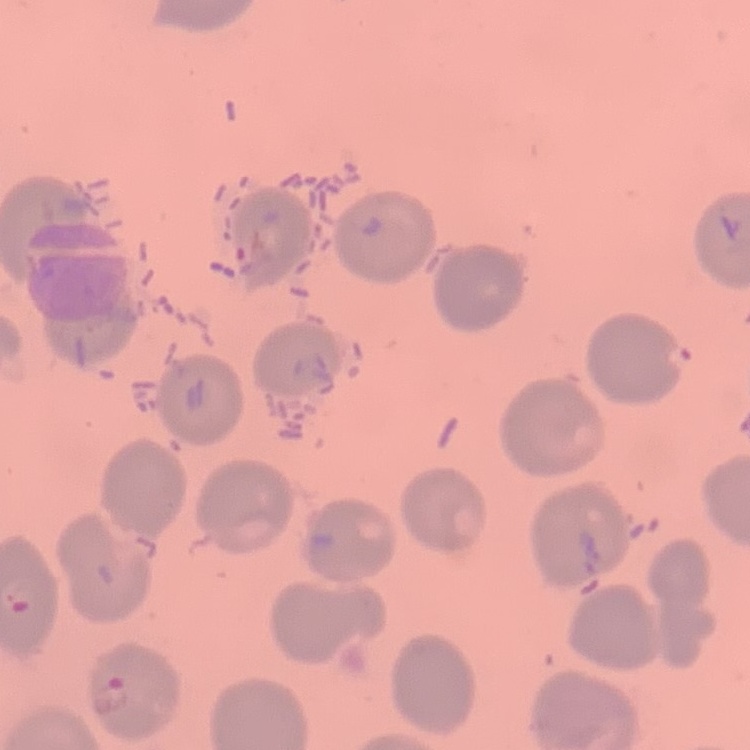

{
  "erythrocyte_morphology": "no rouleaux formation",
  "stain": "Field's or Giemsa",
  "preparation": "thin blood smear",
  "image_type": "one tile cut from a larger photomicrograph"
}